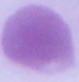

Summary:
  - Magnification: 1000x
  - Identification: erythrocyte
  - Modality: micrograph